Locate every blood parasite and identify its species.
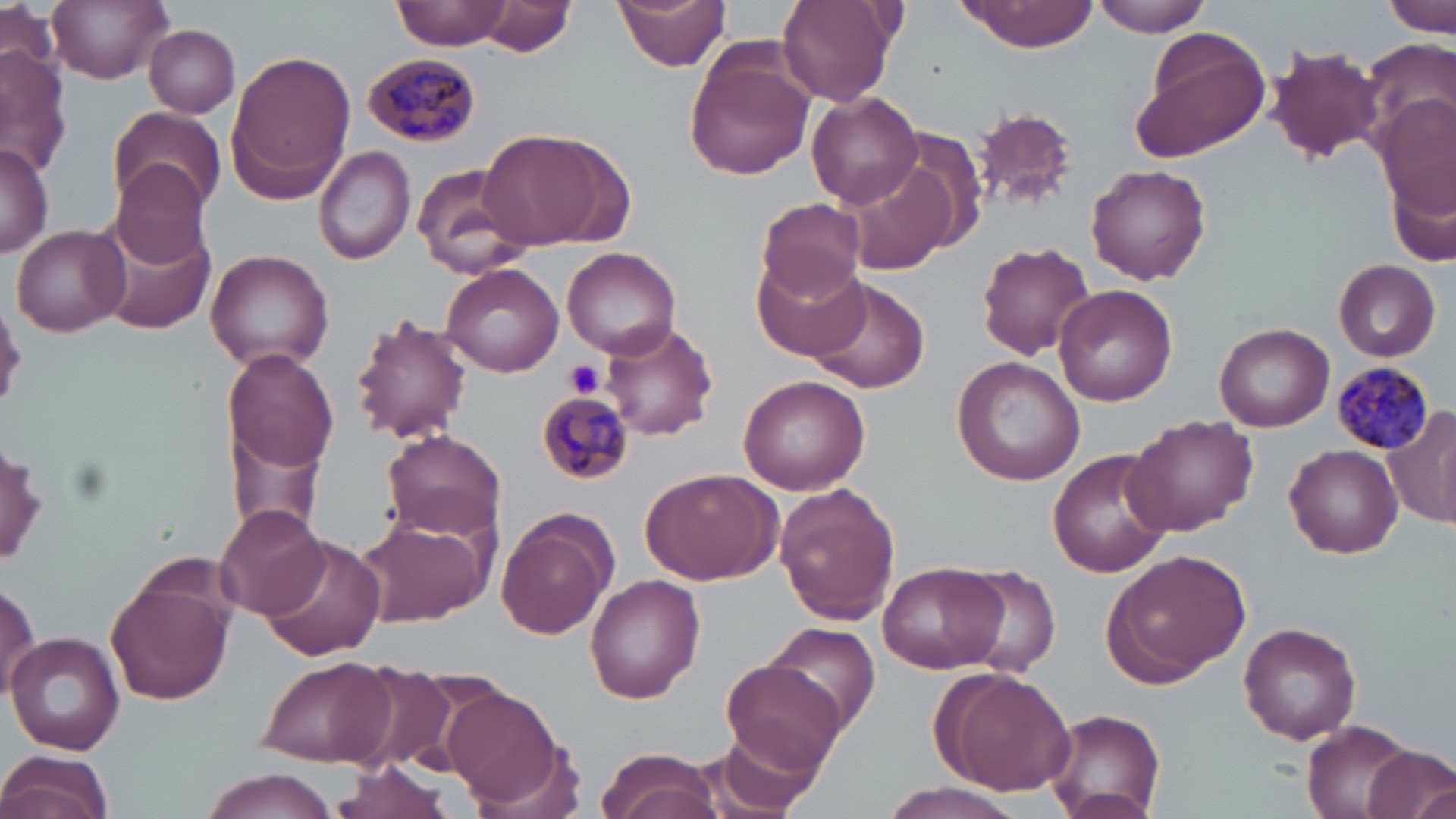

Approximate bounding boxes as [x1, y1, x2, y2] in pixels.
Plasmodium malariae-infected red blood cells: [362, 53, 481, 147], [1330, 358, 1433, 455], [537, 390, 634, 485].
No Plasmodium falciparum, Plasmodium ovale, Plasmodium vivax, Babesia divergens, or Trypanosoma brucei observed.

Uninfected red blood cell locations: [47, 0, 173, 81], [392, 0, 511, 52], [478, 0, 575, 56], [613, 0, 731, 73], [777, 0, 898, 107], [957, 0, 1101, 52], [1090, 0, 1214, 36], [1383, 0, 1454, 37], [1, 4, 61, 79], [144, 23, 241, 118], [1132, 31, 1271, 161], [1360, 39, 1455, 153], [1263, 42, 1387, 164], [0, 44, 74, 174], [684, 44, 815, 183], [224, 51, 355, 204], [807, 91, 922, 208], [1377, 99, 1454, 218], [108, 107, 225, 219], [972, 107, 1080, 211], [477, 127, 631, 250], [0, 142, 53, 259], [314, 144, 416, 266], [1386, 154, 1456, 269], [845, 159, 958, 276], [411, 161, 534, 282], [111, 162, 212, 269], [1087, 164, 1211, 285], [754, 196, 868, 303], [95, 212, 216, 334], [11, 224, 131, 335], [977, 242, 1095, 360], [561, 246, 683, 358], [204, 249, 334, 371], [753, 251, 871, 362], [1333, 259, 1442, 361], [439, 263, 567, 378], [805, 277, 930, 394], [1055, 285, 1178, 405], [348, 314, 473, 446], [601, 321, 719, 441], [1212, 322, 1333, 432], [225, 348, 338, 475], [951, 356, 1085, 485], [738, 374, 871, 494], [220, 405, 334, 542], [1385, 406, 1456, 530], [1123, 416, 1256, 536], [382, 430, 506, 542], [1285, 444, 1403, 557], [1047, 448, 1172, 579], [640, 469, 782, 585], [775, 486, 901, 626], [213, 503, 332, 621], [495, 510, 617, 639], [355, 513, 494, 628], [259, 535, 387, 660], [1104, 546, 1252, 683], [878, 560, 1010, 675], [961, 563, 1060, 674], [104, 567, 236, 709], [0, 573, 41, 705], [584, 574, 706, 700], [1239, 621, 1362, 744], [762, 622, 881, 733], [4, 631, 125, 754], [253, 655, 392, 767], [333, 661, 457, 772], [720, 661, 848, 775], [935, 669, 1077, 795], [440, 681, 570, 811], [1043, 708, 1167, 817], [1302, 719, 1420, 818], [699, 728, 823, 816], [595, 746, 725, 819], [1363, 746, 1456, 819], [0, 749, 114, 819], [330, 759, 454, 819], [200, 767, 340, 819], [877, 780, 1028, 819], [1404, 780, 1452, 819]. Platelet locations: [564, 358, 606, 399]. Slide-level diagnosis: Plasmodium malariae. Thin blood film. May-Grünwald-Giemsa-stained preparation. Image is 1456×819 pixels. 1000x magnification. Optical microscopy. Single field of view.